Assess this cell for malaria.
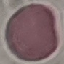
It is uninfected.

Summary:
  - Capture: smartphone camera at the microscope eyepiece
  - Stain: Giemsa
  - Preparation: thin smear
  - Image type: cell patch, automatically extracted from a larger field of view and resized to 64 × 64 pixels